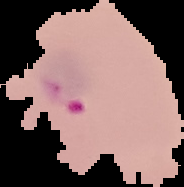 Image is 184×187 pixels. Result: malaria parasites detected. From a thin blood film. Cell region segmented out of the field of view; the surrounding area is masked to black.